Report the malaria status of this cell.
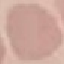

It is uninfected.

Summary:
  - Stain: Giemsa
  - Capture: smartphone through the microscope eyepiece
  - Preparation: thin blood smear
  - Image type: automatically extracted cell patch, resized to 64 × 64 pixels